Give the extent of all Plasmodium malariae-infected red blood cells.
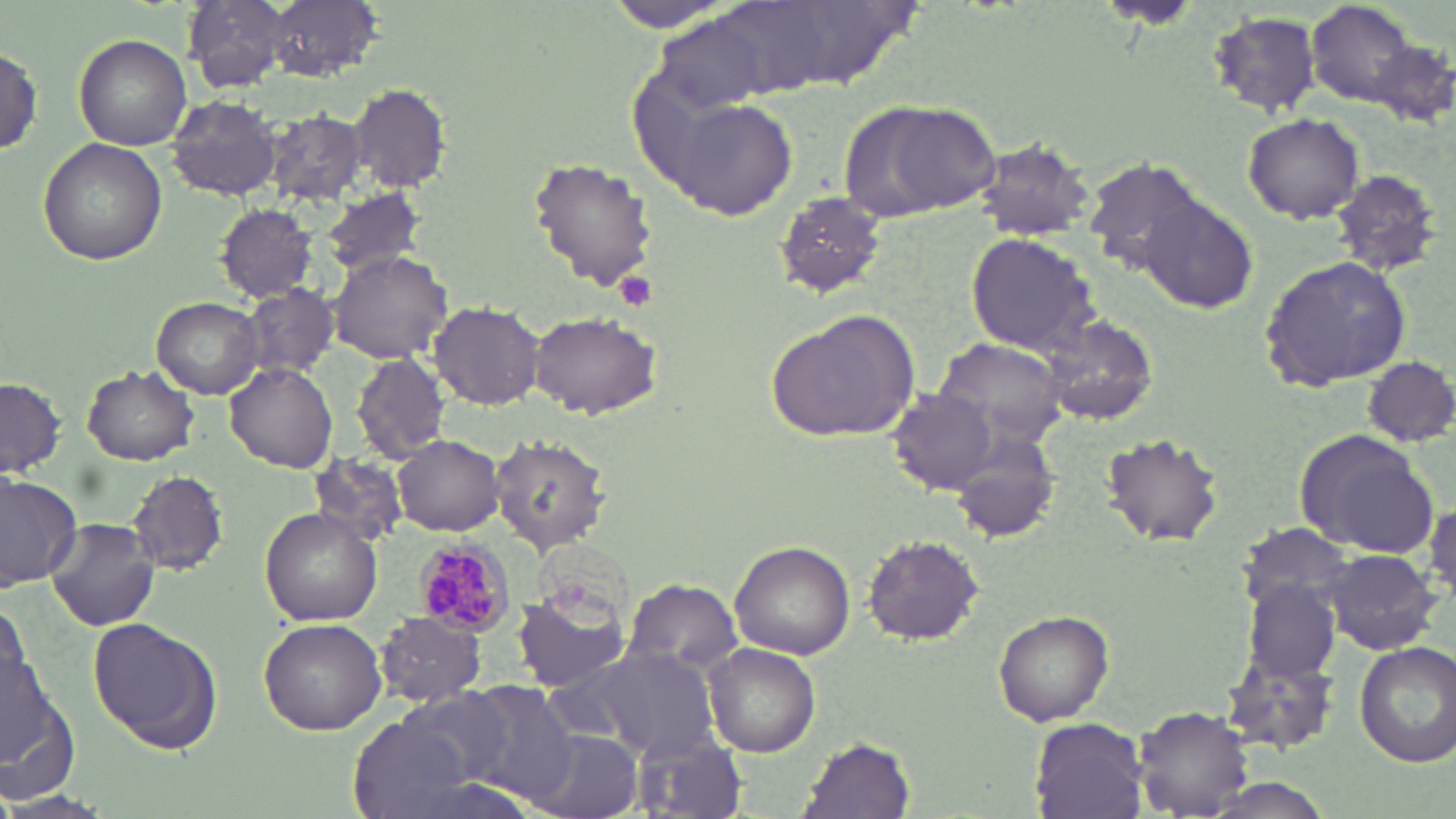

Approximate bounding boxes as named x1/y1/x2/y2 corners in pixels.
Plasmodium malariae-infected red blood cells: (x1=413, y1=539, x2=514, y2=638).

Summary:
  - Uninfected red blood cell locations: (x1=181, y1=1, x2=293, y2=92), (x1=256, y1=1, x2=377, y2=82), (x1=1309, y1=2, x2=1417, y2=105), (x1=602, y1=3, x2=745, y2=34), (x1=1210, y1=10, x2=1325, y2=117), (x1=75, y1=33, x2=193, y2=149), (x1=1369, y1=39, x2=1456, y2=128), (x1=1, y1=41, x2=43, y2=160), (x1=349, y1=83, x2=452, y2=192), (x1=168, y1=96, x2=282, y2=201), (x1=666, y1=97, x2=798, y2=218), (x1=845, y1=100, x2=1003, y2=224), (x1=264, y1=111, x2=366, y2=205), (x1=1244, y1=112, x2=1366, y2=223), (x1=38, y1=137, x2=166, y2=266), (x1=972, y1=139, x2=1097, y2=241), (x1=528, y1=156, x2=659, y2=292), (x1=1082, y1=156, x2=1207, y2=273), (x1=1328, y1=167, x2=1445, y2=277), (x1=320, y1=185, x2=425, y2=278), (x1=775, y1=194, x2=885, y2=297), (x1=1139, y1=197, x2=1258, y2=314), (x1=215, y1=202, x2=316, y2=301), (x1=965, y1=231, x2=1097, y2=354), (x1=329, y1=250, x2=454, y2=364), (x1=1258, y1=256, x2=1414, y2=395), (x1=240, y1=284, x2=339, y2=381), (x1=152, y1=296, x2=265, y2=398), (x1=430, y1=301, x2=543, y2=410), (x1=766, y1=308, x2=921, y2=444), (x1=530, y1=312, x2=659, y2=420), (x1=1039, y1=313, x2=1160, y2=426), (x1=934, y1=335, x2=1071, y2=446), (x1=354, y1=352, x2=449, y2=464), (x1=1359, y1=353, x2=1456, y2=446), (x1=227, y1=362, x2=338, y2=471), (x1=82, y1=364, x2=198, y2=464), (x1=1, y1=377, x2=65, y2=477), (x1=888, y1=389, x2=997, y2=494), (x1=1096, y1=428, x2=1225, y2=546), (x1=1294, y1=430, x2=1434, y2=556), (x1=949, y1=432, x2=1059, y2=544), (x1=392, y1=436, x2=506, y2=536), (x1=490, y1=436, x2=608, y2=553), (x1=305, y1=451, x2=407, y2=549), (x1=0, y1=469, x2=82, y2=590), (x1=126, y1=470, x2=229, y2=576), (x1=1426, y1=500, x2=1455, y2=597), (x1=261, y1=507, x2=383, y2=625), (x1=45, y1=517, x2=155, y2=630), (x1=1237, y1=523, x2=1356, y2=612), (x1=862, y1=534, x2=985, y2=645), (x1=731, y1=542, x2=853, y2=658), (x1=1323, y1=549, x2=1443, y2=655), (x1=621, y1=580, x2=742, y2=678), (x1=1247, y1=580, x2=1340, y2=682), (x1=517, y1=585, x2=631, y2=692), (x1=0, y1=603, x2=31, y2=708), (x1=995, y1=609, x2=1114, y2=726), (x1=376, y1=611, x2=485, y2=706), (x1=87, y1=617, x2=223, y2=756), (x1=259, y1=617, x2=387, y2=735), (x1=1354, y1=640, x2=1456, y2=767), (x1=701, y1=642, x2=820, y2=756), (x1=562, y1=648, x2=721, y2=758), (x1=1221, y1=649, x2=1341, y2=758), (x1=2, y1=668, x2=79, y2=801), (x1=455, y1=680, x2=579, y2=806), (x1=350, y1=697, x2=517, y2=819), (x1=1135, y1=706, x2=1251, y2=815), (x1=1029, y1=717, x2=1151, y2=818), (x1=530, y1=729, x2=645, y2=819), (x1=630, y1=732, x2=745, y2=819), (x1=800, y1=736, x2=916, y2=818)
  - Platelet locations: (x1=616, y1=271, x2=656, y2=309)
  - Slide-level diagnosis: Plasmodium malariae
  - Field of view: one of a larger specimen
  - Modality: light microscopy
  - Preparation: thin blood film
  - Stain: May-Grünwald-Giemsa
  - Magnification: 1000x
  - Image size: 1456×819 pixels